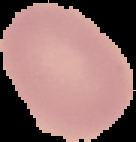

preparation = thin blood film
image size = 136×142 pixels
image type = cell region segmented out of the field of view; surrounding area masked to black
result = negative for Plasmodium parasites